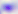

Summary:
  - Identification: Toxoplasma gondii
  - Modality: photomicrograph
  - Magnification: 400x